Classify this cell by malaria status.
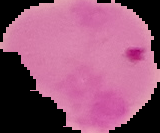
It is parasitized.

Segmented cell region on a black background. From a thin blood film. Image is 160×133 pixels.